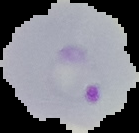

{
  "image_type": "cell region segmented out of the field of view; surrounding area masked to black",
  "malaria_status": "parasitized",
  "image_size": "139×133 pixels",
  "preparation": "thin blood film"
}